Rate the background quality.
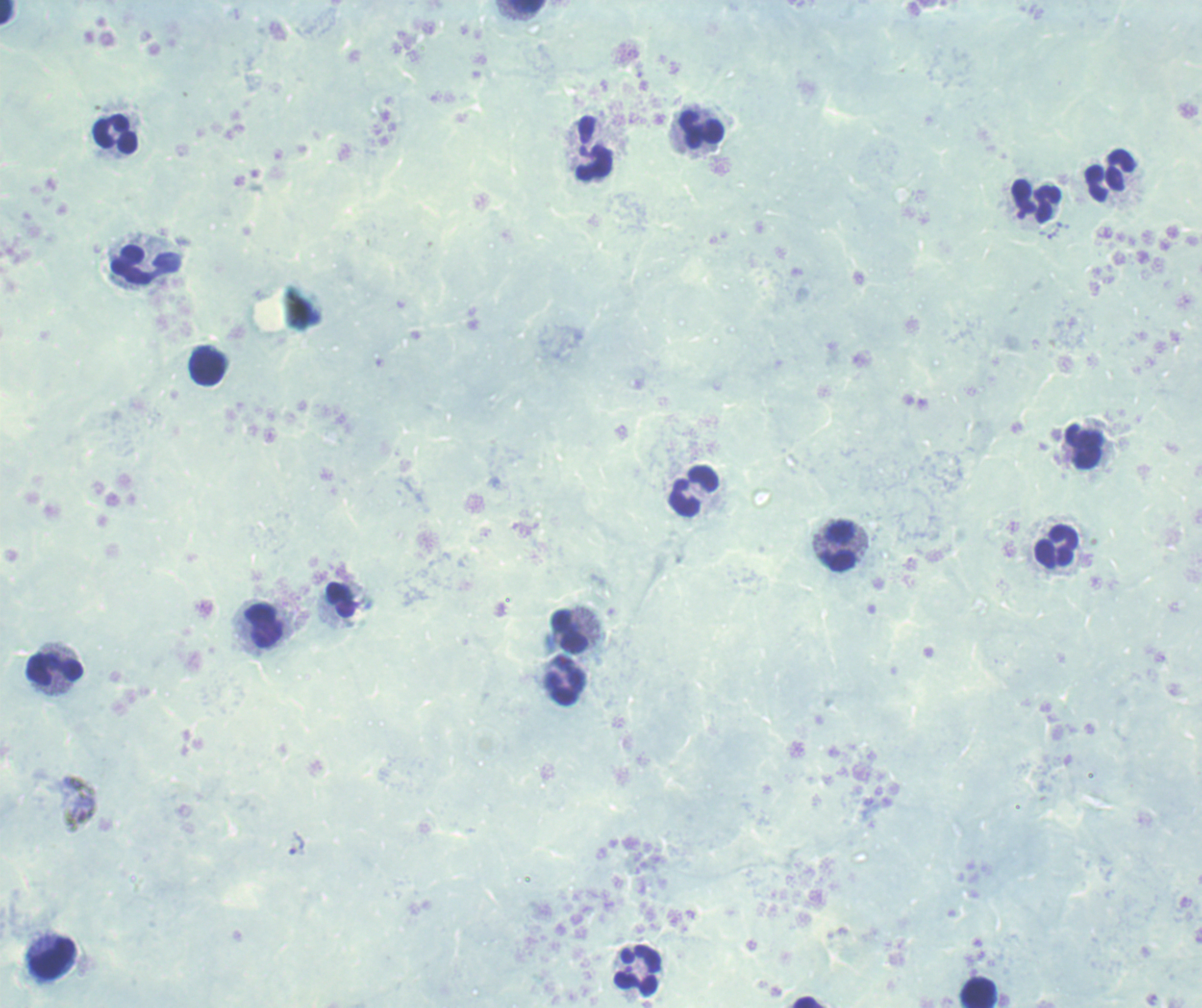

Poor.

Approximate object centers, in pixels from the top-left corner. Leukocyte locations: (x=527, y=7), (x=6, y=13), (x=701, y=131), (x=116, y=135), (x=594, y=148), (x=1111, y=177), (x=1036, y=201), (x=147, y=265), (x=208, y=368), (x=1084, y=448), (x=695, y=492), (x=836, y=545), (x=1056, y=547), (x=263, y=625), (x=567, y=632), (x=54, y=669), (x=567, y=681), (x=51, y=957), (x=638, y=971), (x=978, y=991), (x=806, y=1003). Thick blood film. Previously used in a real diagnosis. Result: no Plasmodium parasites detected. Captured at 100x magnification. Romanowsky stain. Single field of view. Image is 1202×1008 pixels.